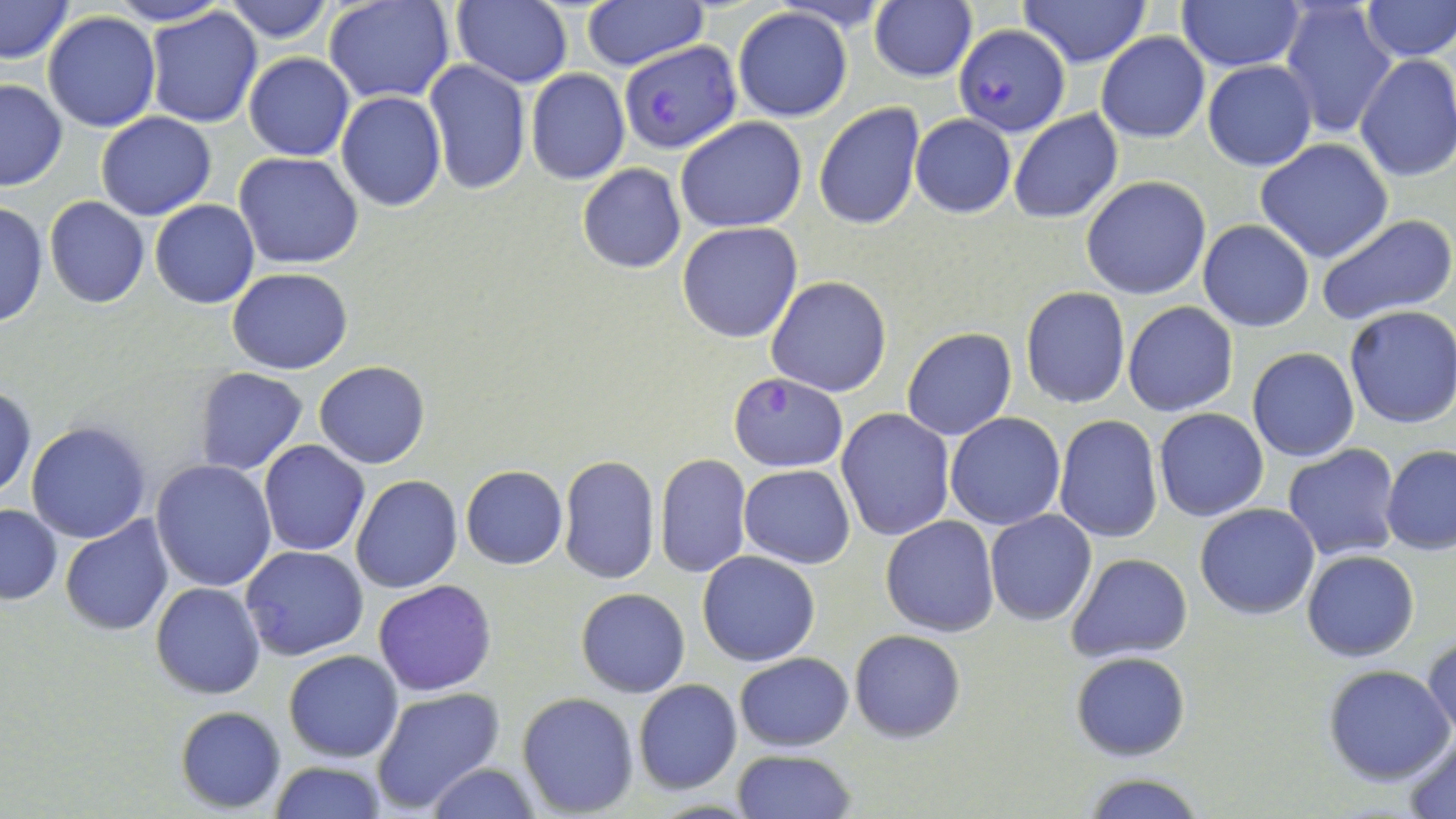

slide_level_diagnosis: Plasmodium falciparum
magnification: 1000x
modality: light microscopy
field_of_view: one of a larger specimen
uninfected_red_blood_cell_locations_subset: 'approximate bounding boxes as named x1/y1/x2/y2 corners in pixels: (x1=1, y1=0, x2=76, y2=63), (x1=104, y1=0, x2=231, y2=27), (x1=222, y1=0, x2=334, y2=43), (x1=453, y1=0, x2=573, y2=88), (x1=580, y1=0, x2=708, y2=70), (x1=1015, y1=0, x2=1152, y2=67), (x1=1177, y1=0, x2=1305, y2=72), (x1=1279, y1=0, x2=1398, y2=140), (x1=1360, y1=0, x2=1455, y2=62), (x1=323, y1=1, x2=456, y2=105), (x1=869, y1=3, x2=977, y2=82), (x1=144, y1=7, x2=264, y2=128), (x1=733, y1=8, x2=853, y2=121), (x1=42, y1=9, x2=161, y2=132), (x1=1097, y1=33, x2=1209, y2=143), (x1=242, y1=52, x2=355, y2=161), (x1=1354, y1=54, x2=1456, y2=182), (x1=424, y1=60, x2=530, y2=196), (x1=1203, y1=61, x2=1317, y2=171), (x1=525, y1=68, x2=631, y2=184), (x1=0, y1=78, x2=68, y2=193), (x1=335, y1=91, x2=446, y2=211), (x1=812, y1=102, x2=926, y2=231), (x1=1008, y1=109, x2=1123, y2=224), (x1=95, y1=111, x2=217, y2=220), (x1=910, y1=115, x2=1016, y2=218), (x1=675, y1=116, x2=807, y2=234), (x1=1255, y1=139, x2=1394, y2=263), (x1=233, y1=152, x2=365, y2=271), (x1=577, y1=163, x2=686, y2=274), (x1=1081, y1=176, x2=1211, y2=299), (x1=44, y1=196, x2=150, y2=309), (x1=0, y1=200, x2=50, y2=330), (x1=150, y1=200, x2=260, y2=309), (x1=1315, y1=212, x2=1456, y2=325), (x1=1197, y1=220, x2=1316, y2=333), (x1=677, y1=222, x2=802, y2=343), (x1=227, y1=267, x2=353, y2=375), (x1=766, y1=276, x2=892, y2=397), (x1=1020, y1=287, x2=1131, y2=409), (x1=1122, y1=302, x2=1238, y2=416), (x1=1343, y1=306, x2=1456, y2=429), (x1=902, y1=327, x2=1016, y2=440), (x1=1248, y1=347, x2=1360, y2=463), (x1=314, y1=361, x2=430, y2=469), (x1=192, y1=368, x2=308, y2=476), (x1=1, y1=384, x2=37, y2=499), (x1=837, y1=408, x2=957, y2=542), (x1=1153, y1=408, x2=1269, y2=522), (x1=945, y1=413, x2=1066, y2=530), (x1=1053, y1=416, x2=1163, y2=543), (x1=26, y1=421, x2=151, y2=543), (x1=259, y1=441, x2=369, y2=556), (x1=1282, y1=445, x2=1401, y2=562), (x1=1381, y1=445, x2=1456, y2=555), (x1=557, y1=454, x2=660, y2=586), (x1=655, y1=454, x2=752, y2=577), (x1=150, y1=459, x2=277, y2=592), (x1=738, y1=464, x2=855, y2=567), (x1=461, y1=465, x2=568, y2=569), (x1=351, y1=475, x2=462, y2=593), (x1=1, y1=503, x2=61, y2=604), (x1=1195, y1=503, x2=1321, y2=619), (x1=984, y1=511, x2=1097, y2=626), (x1=881, y1=515, x2=1000, y2=637), (x1=60, y1=517, x2=175, y2=637), (x1=241, y1=545, x2=368, y2=660), (x1=697, y1=550, x2=821, y2=666), (x1=1301, y1=550, x2=1419, y2=661), (x1=1065, y1=552, x2=1194, y2=663), (x1=372, y1=580, x2=497, y2=696), (x1=150, y1=582, x2=267, y2=700), (x1=576, y1=588, x2=690, y2=697), (x1=850, y1=629, x2=965, y2=742), (x1=1424, y1=633, x2=1455, y2=745), (x1=283, y1=649, x2=403, y2=761), (x1=1071, y1=651, x2=1191, y2=762), (x1=735, y1=653, x2=853, y2=751), (x1=1322, y1=664, x2=1456, y2=784), (x1=633, y1=679, x2=742, y2=794), (x1=371, y1=687, x2=503, y2=815), (x1=517, y1=691, x2=639, y2=814), (x1=175, y1=706, x2=286, y2=811), (x1=1401, y1=730, x2=1456, y2=816), (x1=732, y1=749, x2=855, y2=819), (x1=268, y1=761, x2=387, y2=818), (x1=424, y1=763, x2=541, y2=819), (x1=1078, y1=773, x2=1207, y2=819)'
image_size: 1456×819 pixels
plasmodium_falciparum_infected_red_blood_cell_locations_subset: 'approximate bounding boxes as named x1/y1/x2/y2 corners in pixels: (x1=619, y1=41, x2=742, y2=152), (x1=729, y1=374, x2=848, y2=471)'
preparation: thin blood film
stain: May-Grünwald-Giemsa